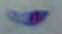
Summary:
  - Modality: photomicrograph
  - Identification: Toxoplasma gondii
  - Magnification: 1000x